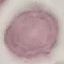
{
  "result": "no malaria parasites detected",
  "stain": "Giemsa",
  "capture": "smartphone camera at the microscope eyepiece",
  "image_type": "automatically extracted cell patch, resized to 64 × 64 pixels",
  "preparation": "thin blood film"
}